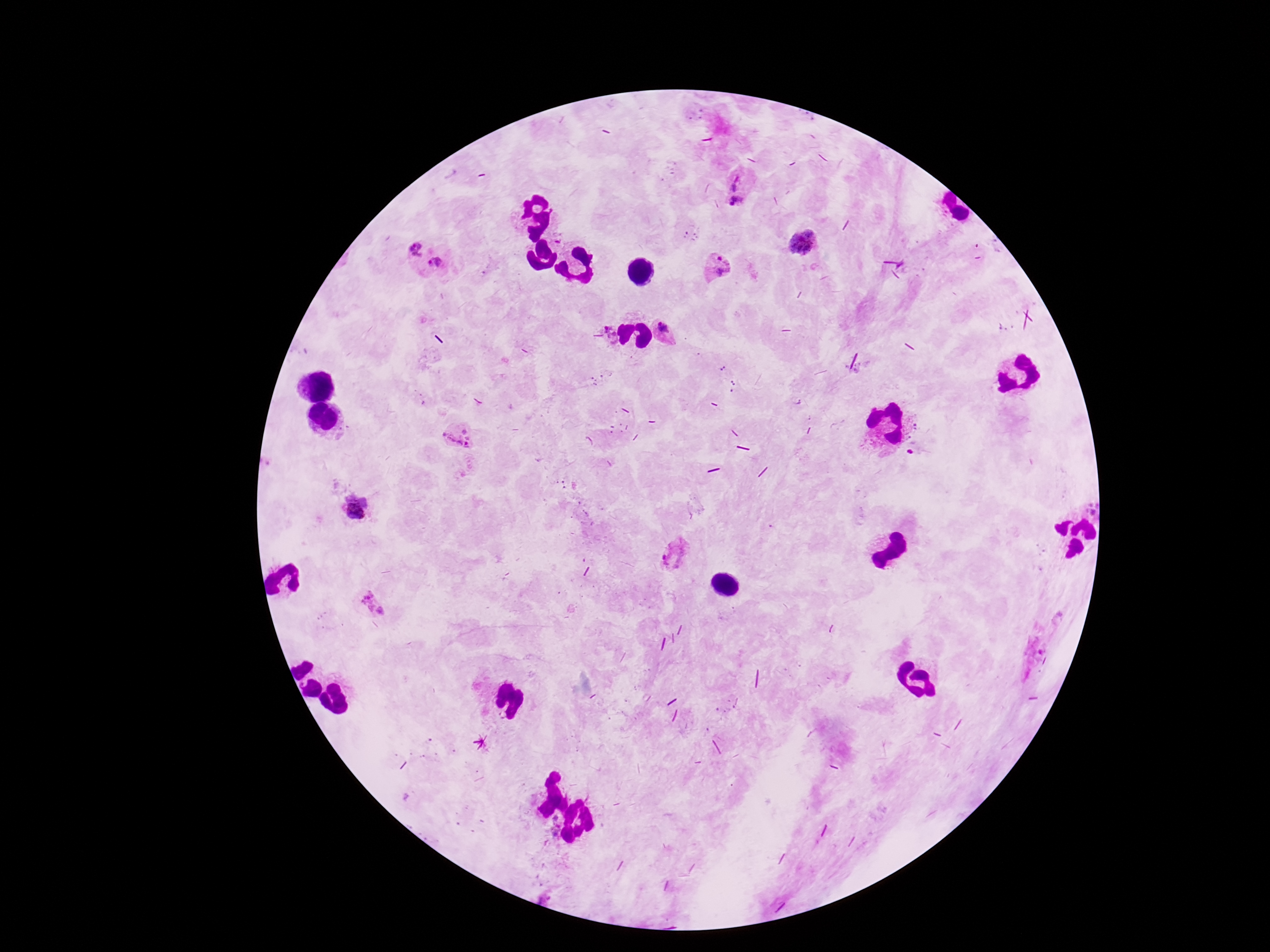

Approximate centers as [x, y] in pixels.
Summary:
  - Plasmodium parasite locations: [734, 190], [799, 240], [411, 251], [438, 265], [718, 267], [666, 329], [609, 333], [455, 436], [357, 510], [672, 556], [374, 605]
  - Patient malaria status: positive
  - Image size: 1270×952 pixels
  - Preparation: thick peripheral-blood smear
  - Capture: smartphone camera through the microscope eyepiece
  - Magnification: 100x
  - Field of view: one from this slide
  - Stain: Giemsa